Outline each Plasmodium falciparum-infected red blood cell.
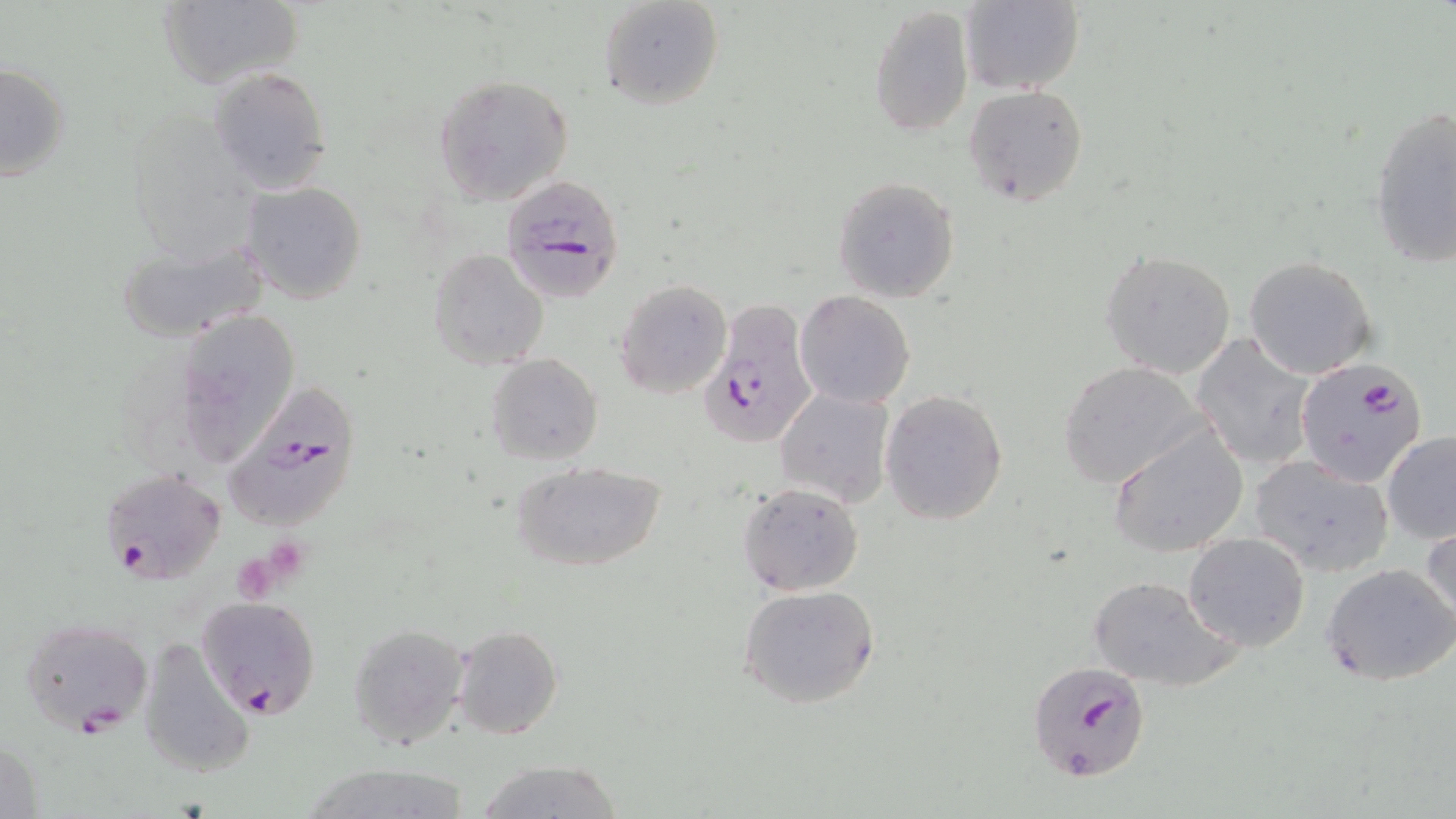
Approximate bounding boxes as (x1, y1, x2, y2) in pixels.
Plasmodium falciparum-infected red blood cells: (502, 176, 630, 309), (699, 301, 817, 452), (1297, 356, 1429, 487), (222, 383, 365, 531), (99, 468, 225, 588), (197, 597, 320, 717), (20, 616, 154, 736), (1026, 663, 1146, 784).

{
  "slide_level_diagnosis": "Plasmodium falciparum",
  "uninfected_red_blood_cell_locations": "approximate bounding boxes as (x1, y1, x2, y2) in pixels: (156, 0, 304, 89), (598, 0, 725, 110), (960, 0, 1084, 95), (867, 4, 973, 140), (1, 62, 71, 181), (209, 65, 333, 193), (430, 73, 574, 207), (963, 84, 1089, 207), (1368, 103, 1455, 270), (832, 177, 960, 303), (240, 181, 367, 304), (115, 239, 266, 340), (428, 249, 548, 370), (1100, 249, 1237, 379), (1244, 256, 1378, 379), (614, 278, 733, 398), (795, 291, 916, 408), (175, 308, 300, 469), (1190, 333, 1320, 470), (486, 355, 603, 465), (1057, 361, 1207, 487), (776, 385, 896, 510), (880, 389, 1008, 525), (1108, 425, 1250, 558), (1381, 431, 1456, 544), (1248, 456, 1396, 576), (511, 462, 667, 574), (737, 482, 864, 597), (1422, 520, 1455, 633), (1183, 531, 1311, 650), (1322, 562, 1456, 686), (1088, 573, 1242, 691), (737, 584, 881, 711), (348, 623, 471, 750), (452, 624, 563, 740), (139, 636, 255, 779), (472, 759, 625, 819)",
  "stain": "May-Grünwald-Giemsa",
  "magnification": "1000x",
  "preparation": "thin blood smear",
  "image_size": "1456×819 pixels",
  "platelet_locations": "approximate bounding boxes as (x1, y1, x2, y2) in pixels: (265, 537, 310, 579), (231, 559, 280, 603)",
  "field_of_view": "single",
  "modality": "light microscopy"
}